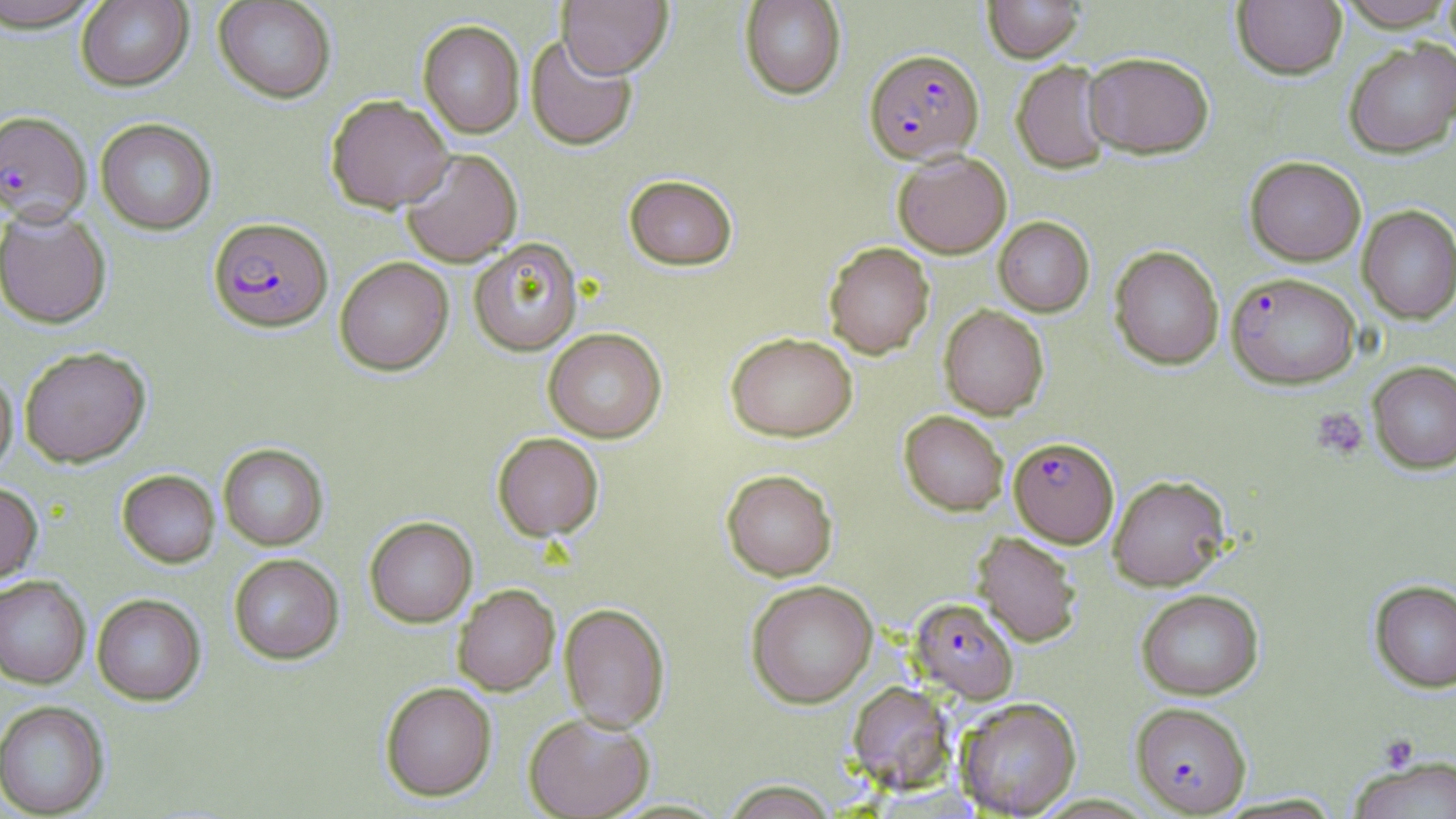 Approximate bounding boxes as (x1,y1)-(x2,y2) corner pairs in pixels. Uninfected red blood cell locations: (1,0)-(107,32), (75,0)-(193,91), (213,0)-(337,103), (557,0)-(673,78), (739,0)-(846,100), (982,0)-(1085,62), (1232,1)-(1347,79), (1336,1)-(1456,30), (418,20)-(525,138), (524,34)-(638,151), (1344,38)-(1456,158), (1083,51)-(1214,159), (1011,60)-(1114,174), (326,95)-(454,213), (95,118)-(217,235), (400,148)-(523,267), (892,150)-(1012,258), (1244,156)-(1366,266), (624,174)-(737,271), (0,206)-(112,329), (1357,206)-(1456,323), (993,216)-(1094,316), (468,238)-(583,356), (824,241)-(934,359), (1109,245)-(1224,370), (335,257)-(453,376), (938,304)-(1049,419), (542,327)-(667,442), (725,332)-(858,441), (19,346)-(151,468), (1368,361)-(1456,473), (0,369)-(18,480), (899,410)-(1008,516), (492,432)-(604,542), (218,443)-(328,550), (721,469)-(838,580), (117,470)-(220,568), (1107,474)-(1231,590), (0,482)-(43,584), (364,516)-(477,627), (972,532)-(1082,647), (228,554)-(344,665), (0,576)-(91,689), (745,579)-(878,708), (1369,579)-(1456,692), (452,584)-(560,695), (1136,588)-(1264,699), (92,594)-(206,706), (559,603)-(670,733), (380,681)-(497,801), (847,682)-(957,794), (955,697)-(1081,817), (0,700)-(110,818), (523,713)-(655,819), (1347,756)-(1456,818), (721,780)-(839,819). Platelet locations: (1311,408)-(1368,460), (1378,733)-(1419,772). Plasmodium falciparum-infected red blood cell locations: (864,48)-(984,164), (0,110)-(93,225), (208,218)-(332,332), (1226,272)-(1361,389), (1009,437)-(1119,547), (909,597)-(1018,703), (1130,701)-(1252,816). Slide-level diagnosis: Plasmodium falciparum. Optical microscopy. May-Grünwald-Giemsa-stained preparation. Image is 1456×819 pixels. One field of a larger specimen. Captured at 1000x magnification. Thin blood film.